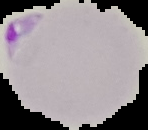

Summary:
  - Malaria status: parasitized
  - Image type: cell region segmented out of the field of view; surrounding area masked to black
  - Preparation: thin blood film
  - Image size: 148×130 pixels